State the blood parasite species.
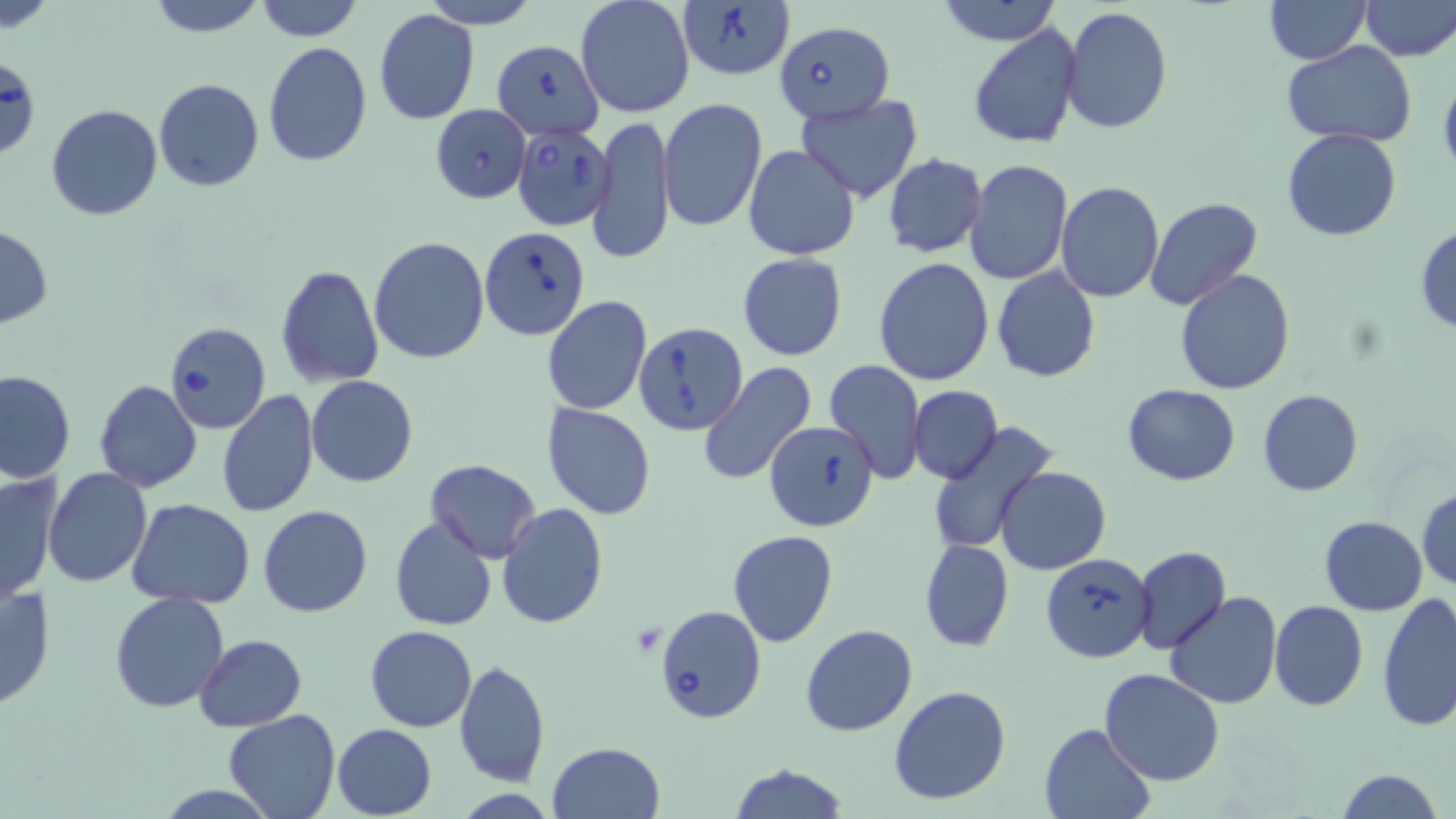
Babesia divergens.

Summary:
  - Coordinate format: approximate bounding boxes as named x1/y1/x2/y2 corners in pixels
  - Platelet locations: (x1=630, y1=624, x2=665, y2=656)
  - Uninfected red blood cell locations: (x1=3, y1=0, x2=57, y2=34), (x1=144, y1=0, x2=269, y2=36), (x1=253, y1=0, x2=365, y2=41), (x1=424, y1=0, x2=541, y2=26), (x1=576, y1=0, x2=695, y2=120), (x1=935, y1=0, x2=1061, y2=46), (x1=1264, y1=0, x2=1368, y2=65), (x1=1358, y1=0, x2=1455, y2=61), (x1=1061, y1=5, x2=1172, y2=134), (x1=373, y1=10, x2=480, y2=125), (x1=968, y1=23, x2=1084, y2=150), (x1=1283, y1=40, x2=1418, y2=149), (x1=262, y1=42, x2=373, y2=167), (x1=153, y1=78, x2=264, y2=192), (x1=796, y1=95, x2=922, y2=202), (x1=658, y1=99, x2=769, y2=233), (x1=46, y1=103, x2=162, y2=220), (x1=589, y1=114, x2=676, y2=265), (x1=1282, y1=128, x2=1400, y2=242), (x1=742, y1=145, x2=859, y2=261), (x1=882, y1=153, x2=987, y2=258), (x1=963, y1=159, x2=1072, y2=286), (x1=1056, y1=181, x2=1165, y2=302), (x1=1146, y1=197, x2=1263, y2=313), (x1=1, y1=225, x2=52, y2=329), (x1=1414, y1=226, x2=1456, y2=332), (x1=368, y1=236, x2=490, y2=365), (x1=737, y1=252, x2=848, y2=360), (x1=874, y1=258, x2=995, y2=386), (x1=277, y1=263, x2=385, y2=389), (x1=990, y1=267, x2=1101, y2=382), (x1=1174, y1=269, x2=1295, y2=394), (x1=542, y1=295, x2=653, y2=416), (x1=824, y1=360, x2=926, y2=486), (x1=697, y1=362, x2=818, y2=485), (x1=1, y1=370, x2=75, y2=484), (x1=306, y1=376, x2=418, y2=487), (x1=95, y1=381, x2=202, y2=493), (x1=1122, y1=383, x2=1241, y2=485), (x1=908, y1=385, x2=1002, y2=484), (x1=216, y1=389, x2=319, y2=518), (x1=1258, y1=389, x2=1363, y2=496), (x1=541, y1=402, x2=657, y2=521), (x1=925, y1=421, x2=1058, y2=556), (x1=426, y1=459, x2=541, y2=562), (x1=995, y1=466, x2=1112, y2=576), (x1=45, y1=468, x2=151, y2=587), (x1=2, y1=474, x2=62, y2=603), (x1=1416, y1=488, x2=1456, y2=590), (x1=127, y1=498, x2=256, y2=607), (x1=497, y1=503, x2=607, y2=628), (x1=257, y1=505, x2=373, y2=618), (x1=389, y1=515, x2=496, y2=631), (x1=1319, y1=515, x2=1428, y2=615), (x1=726, y1=531, x2=839, y2=648), (x1=920, y1=539, x2=1014, y2=651), (x1=1132, y1=545, x2=1232, y2=655), (x1=1, y1=578, x2=56, y2=713), (x1=110, y1=591, x2=231, y2=713), (x1=1165, y1=592, x2=1282, y2=710), (x1=1376, y1=592, x2=1456, y2=732), (x1=1269, y1=600, x2=1368, y2=711), (x1=801, y1=623, x2=918, y2=737), (x1=366, y1=625, x2=477, y2=732), (x1=193, y1=634, x2=305, y2=731), (x1=455, y1=659, x2=549, y2=788), (x1=1098, y1=669, x2=1225, y2=786), (x1=888, y1=684, x2=1012, y2=805), (x1=224, y1=708, x2=341, y2=819), (x1=1039, y1=721, x2=1157, y2=818), (x1=333, y1=723, x2=438, y2=818), (x1=548, y1=741, x2=666, y2=819), (x1=726, y1=763, x2=850, y2=819), (x1=1336, y1=767, x2=1443, y2=819)
  - Babesia divergens-infected red blood cell locations: (x1=678, y1=1, x2=795, y2=83), (x1=774, y1=20, x2=891, y2=123), (x1=491, y1=40, x2=604, y2=138), (x1=0, y1=64, x2=34, y2=160), (x1=430, y1=105, x2=531, y2=203), (x1=512, y1=124, x2=615, y2=231), (x1=479, y1=228, x2=590, y2=340), (x1=164, y1=322, x2=270, y2=433), (x1=633, y1=322, x2=747, y2=434), (x1=764, y1=420, x2=880, y2=532), (x1=1041, y1=553, x2=1155, y2=663), (x1=656, y1=605, x2=767, y2=723)
  - Modality: light microscopy
  - Image size: 1456×819 pixels
  - Stain: May-Grünwald-Giemsa
  - Field of view: one of a larger specimen
  - Magnification: 1000x
  - Preparation: thin blood film